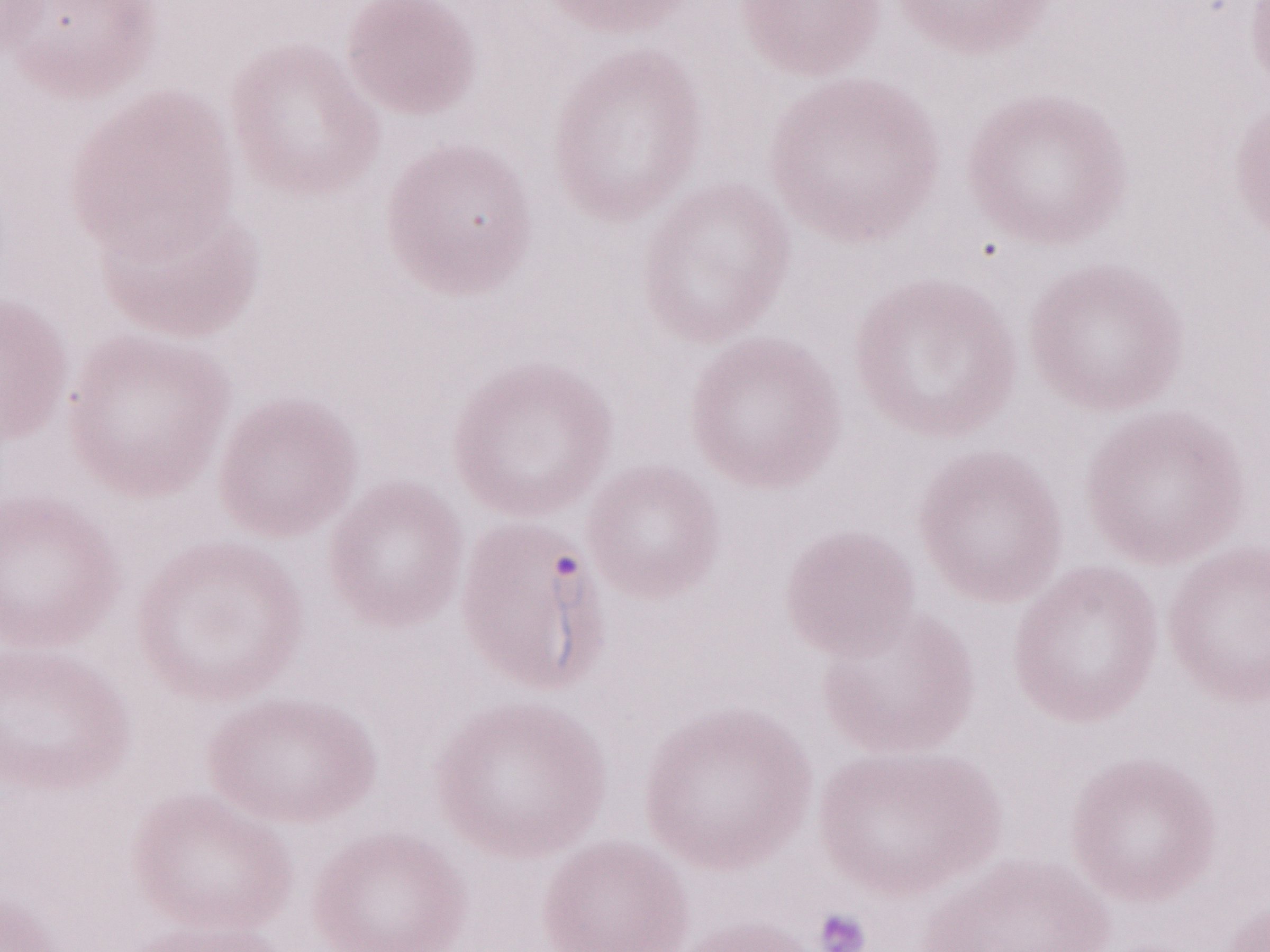

Single field of view. Magnification: 1,000x. May-Grünwald-Giemsa stain. Olympus BX43 microscope and DP73 digital camera. Malaria diagnosis (patient-level): positive. Thin peripheral-blood smear. Image is 1270×952 pixels.